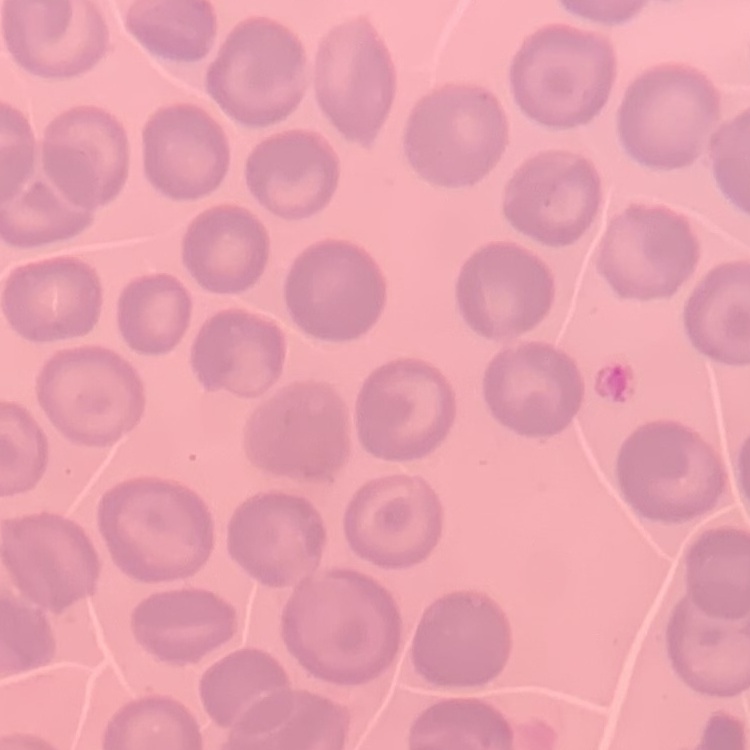
red blood cell morphology = no rouleaux formation
stain = Field's or Giemsa
preparation = thin blood film
image type = square crop of a larger photomicrograph